Report the malaria status of this cell.
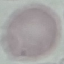
It is uninfected.

image type = automatically extracted cell patch, resized to 64 × 64 pixels
capture = smartphone camera at the microscope eyepiece
stain = Giemsa
preparation = thin blood smear